Classify this cell by malaria status.
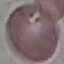

Uninfected.

Summary:
  - Capture: smartphone camera at the microscope eyepiece
  - Preparation: thin blood film
  - Stain: Giemsa
  - Image type: cell patch, automatically extracted from a larger field of view and resized to 64 × 64 pixels